State the blood parasite species.
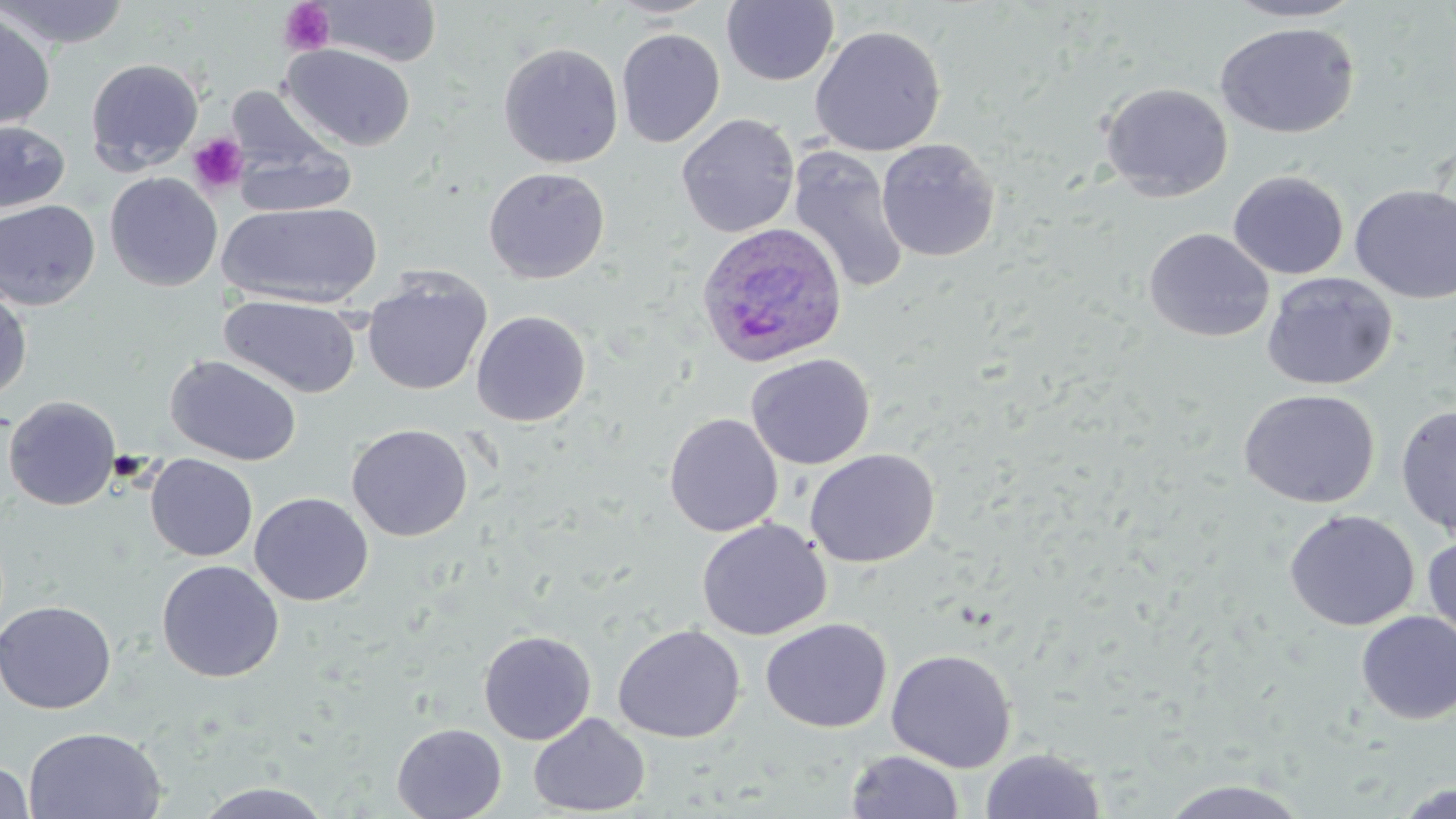
Plasmodium ovale.

image size = 1456×819 pixels
modality = light microscopy
platelet locations = approximate bounding boxes as (x1, y1, x2, y2) in pixels: (279, 1, 336, 56), (187, 132, 250, 196)
Plasmodium ovale-infected red blood cell locations = approximate bounding boxes as (x1, y1, x2, y2) in pixels: (695, 222, 848, 369)
preparation = thin blood film
uninfected red blood cell locations = approximate bounding boxes as (x1, y1, x2, y2) in pixels: (1, 0, 131, 49), (606, 0, 721, 19), (1222, 0, 1368, 22), (317, 1, 443, 67), (721, 1, 839, 86), (0, 8, 56, 132), (1215, 22, 1360, 139), (809, 25, 946, 157), (616, 28, 725, 148), (498, 42, 624, 168), (280, 44, 416, 151), (85, 57, 205, 174), (1099, 82, 1233, 201), (676, 113, 800, 237), (0, 119, 71, 215), (231, 137, 357, 219), (875, 138, 1000, 262), (786, 146, 910, 295), (483, 167, 610, 284), (1228, 170, 1349, 279), (104, 171, 223, 291), (1349, 184, 1456, 303), (0, 199, 101, 311), (217, 202, 382, 307), (1144, 228, 1274, 343), (1261, 271, 1398, 391), (363, 274, 491, 396), (0, 283, 32, 404), (219, 295, 361, 398), (471, 310, 591, 426), (745, 353, 875, 469), (165, 354, 302, 465), (1239, 389, 1380, 509), (3, 395, 121, 510), (1396, 404, 1456, 537), (663, 412, 783, 537), (346, 424, 473, 541), (804, 448, 940, 568), (145, 454, 258, 561), (249, 491, 373, 606), (1283, 509, 1419, 631), (696, 518, 831, 640), (1422, 534, 1455, 644), (156, 559, 284, 682), (0, 600, 117, 714), (1356, 611, 1456, 724), (761, 618, 892, 733), (613, 624, 745, 743), (478, 630, 596, 744), (886, 649, 1017, 772), (528, 713, 650, 816), (391, 723, 506, 819), (23, 726, 166, 818), (980, 747, 1106, 819), (846, 750, 964, 818), (0, 760, 35, 819), (1159, 778, 1311, 818), (193, 781, 336, 818), (1393, 782, 1455, 819)
field of view = one of a larger specimen
stain = May-Grünwald-Giemsa
magnification = 1000x